Locate every blood parasite and identify its species.
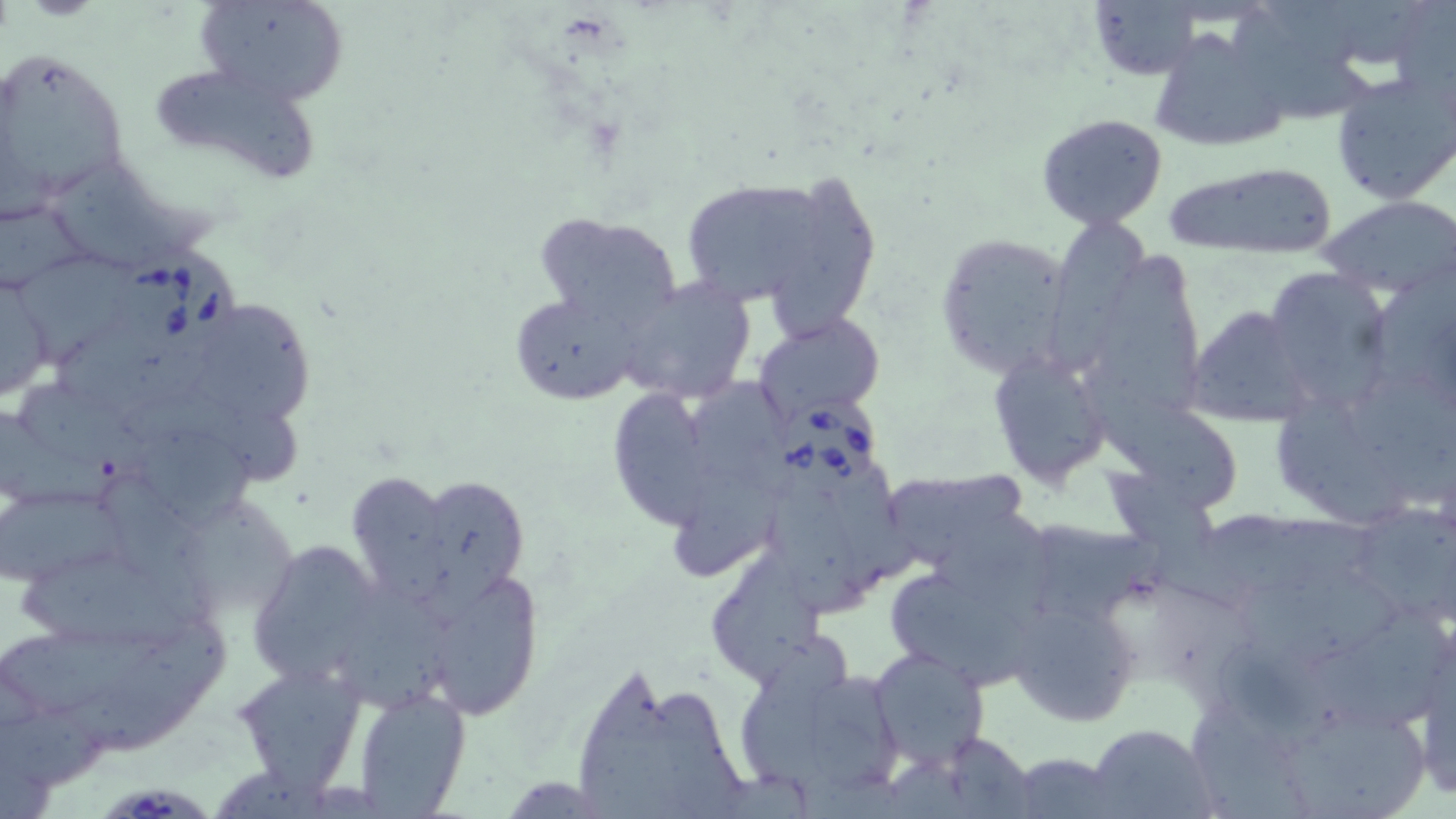

Approximate bounding boxes as (x1, y1, x2, y2) in pixels.
Babesia divergens-infected red blood cells: (117, 249, 249, 360), (775, 397, 881, 497), (104, 783, 212, 819).
No Plasmodium falciparum, Plasmodium ovale, Plasmodium malariae, Plasmodium vivax, or Trypanosoma brucei observed.

slide-level diagnosis = Babesia divergens
preparation = thin blood film
field of view = one of a larger specimen
image size = 1456×819 pixels
modality = light microscopy
magnification = 1000x
uninfected red blood cell locations = approximate bounding boxes as (x1, y1, x2, y2) in pixels: (199, 0, 347, 108), (1089, 0, 1203, 80), (1339, 3, 1420, 66), (1234, 9, 1372, 119), (1146, 28, 1289, 155), (3, 52, 127, 216), (143, 62, 319, 186), (1332, 73, 1456, 204), (1035, 112, 1170, 229), (54, 158, 220, 268), (1164, 162, 1340, 257), (675, 172, 843, 312), (769, 174, 874, 341), (1322, 196, 1456, 297), (2, 206, 111, 287), (532, 212, 682, 330), (1048, 216, 1140, 369), (936, 233, 1073, 379), (1098, 241, 1210, 412), (16, 260, 139, 363), (1272, 267, 1389, 404), (1375, 267, 1456, 360), (615, 279, 756, 404), (0, 280, 53, 406), (508, 288, 641, 406), (194, 299, 324, 424), (1183, 305, 1315, 425), (755, 313, 885, 425), (61, 330, 223, 412), (986, 350, 1113, 489), (1083, 364, 1233, 509), (1356, 369, 1456, 499), (677, 377, 795, 485), (18, 381, 150, 469), (615, 385, 706, 531), (1273, 389, 1408, 527), (124, 391, 301, 483), (0, 411, 128, 501), (137, 426, 257, 524), (1093, 462, 1245, 586), (678, 465, 779, 577), (834, 466, 921, 579), (346, 467, 454, 603), (892, 468, 1027, 565), (99, 470, 210, 625), (412, 473, 530, 602), (0, 490, 127, 582), (771, 490, 867, 621), (187, 498, 294, 608), (1365, 504, 1452, 622), (935, 506, 1064, 613), (1203, 511, 1380, 587), (1039, 518, 1162, 625), (246, 536, 387, 690), (705, 548, 824, 690), (24, 553, 193, 652), (1237, 566, 1402, 663), (436, 573, 540, 723), (890, 574, 1033, 688), (331, 580, 463, 719), (1010, 597, 1142, 726), (1302, 604, 1448, 727), (64, 616, 231, 757), (0, 623, 162, 710), (1221, 640, 1342, 752), (870, 648, 989, 770), (736, 654, 910, 801), (231, 660, 370, 795), (580, 669, 685, 819), (650, 682, 747, 819), (352, 686, 471, 817), (1192, 704, 1308, 819), (0, 707, 103, 788), (1290, 707, 1437, 818), (1087, 725, 1216, 819), (941, 731, 1034, 817), (1010, 751, 1120, 818), (220, 772, 332, 819)
stain = May-Grünwald-Giemsa